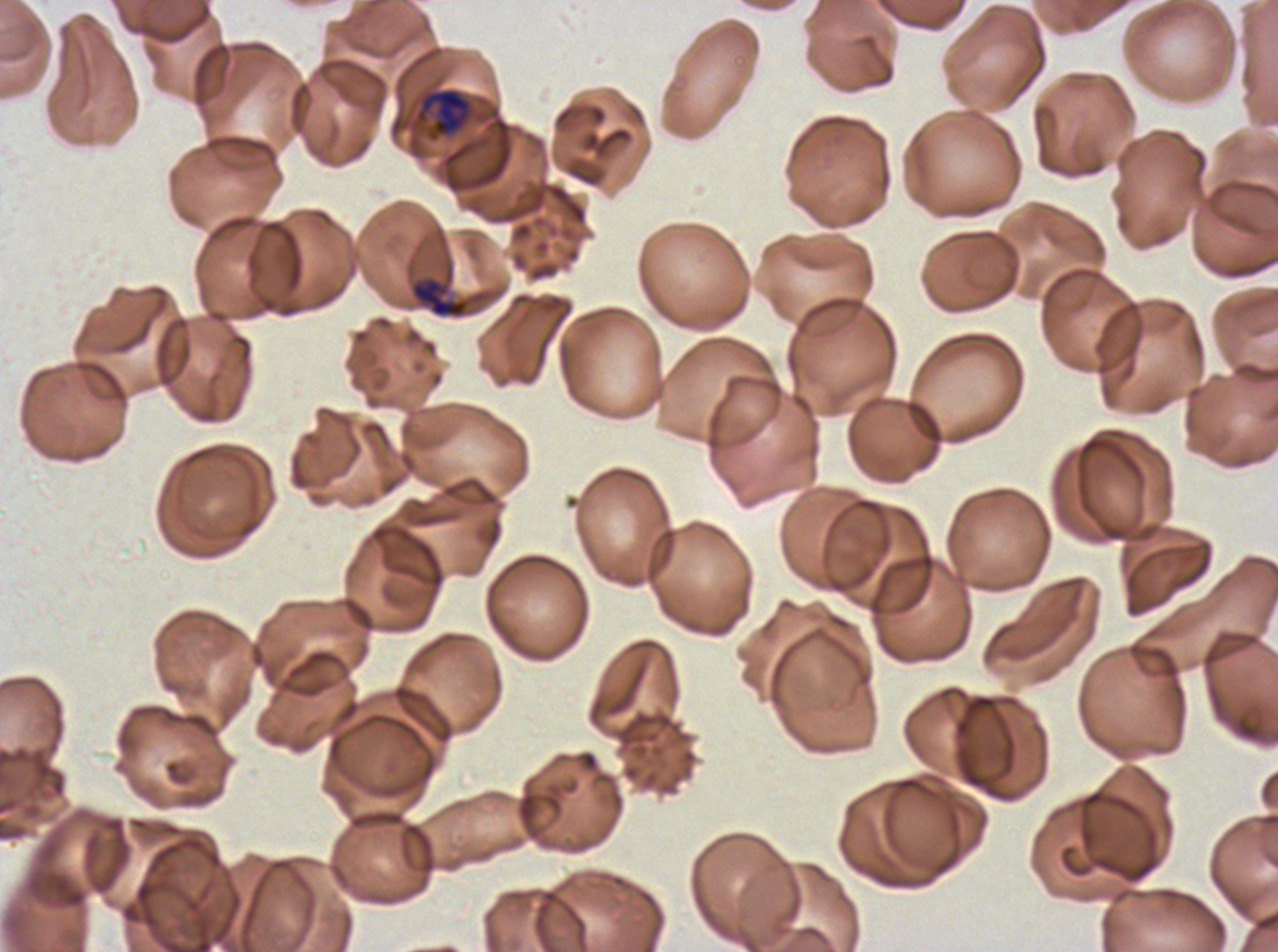

preparation: thin blood film
early_schizont_locations: 'approximate bounding boxes as {x1, y1, x2, y2} in pixels: {413, 87, 476, 143}'
image_size: 1278×952 pixels
specimen: P. falciparum from a patient in The Gambia, cultured ex vivo for 24 to 48 hours
late_ring_early_trophozoite_locations: 'approximate bounding boxes as {x1, y1, x2, y2} in pixels: {410, 276, 469, 318}'
stain: Giemsa
field_of_view: sub-image separated from a larger composite
life_cycle_stages_observed: late-ring/early-trophozoite, early schizont